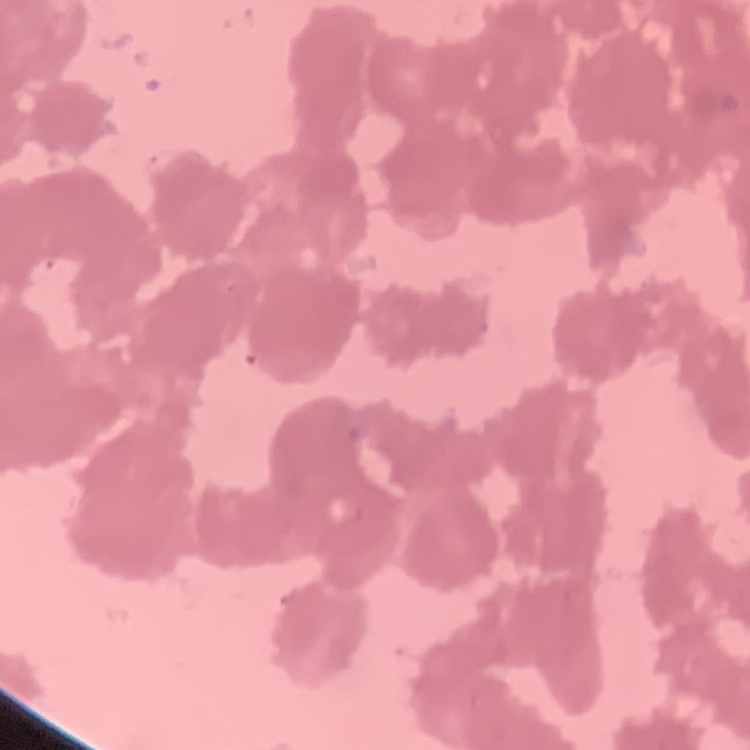 The red blood cells show rouleaux formation. Square crop of a larger photomicrograph. Field's or Giemsa stain. Thin blood smear.